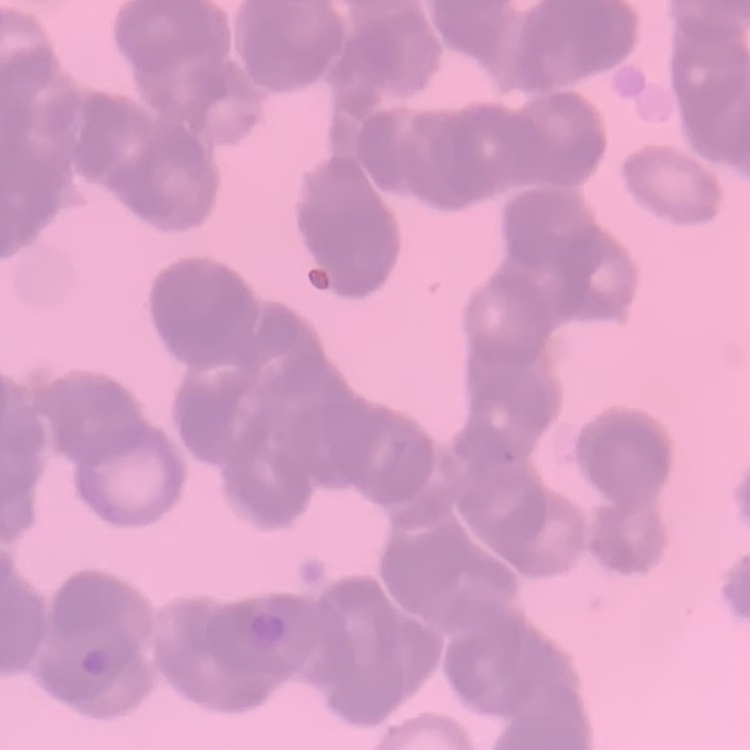 The erythrocytes exhibit rouleaux formation. One tile cut from a larger photomicrograph. Stained with either Field's or Giemsa. Thin blood smear.